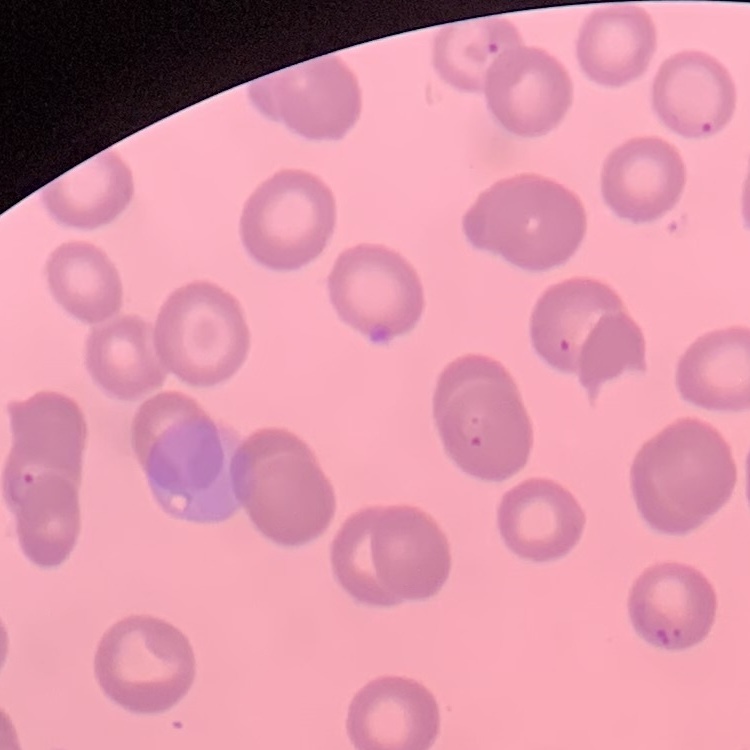

Summary:
  - Red blood cell morphology: no rouleaux formation
  - Stain: Field's or Giemsa
  - Preparation: thin blood smear
  - Image type: square crop of a larger photomicrograph